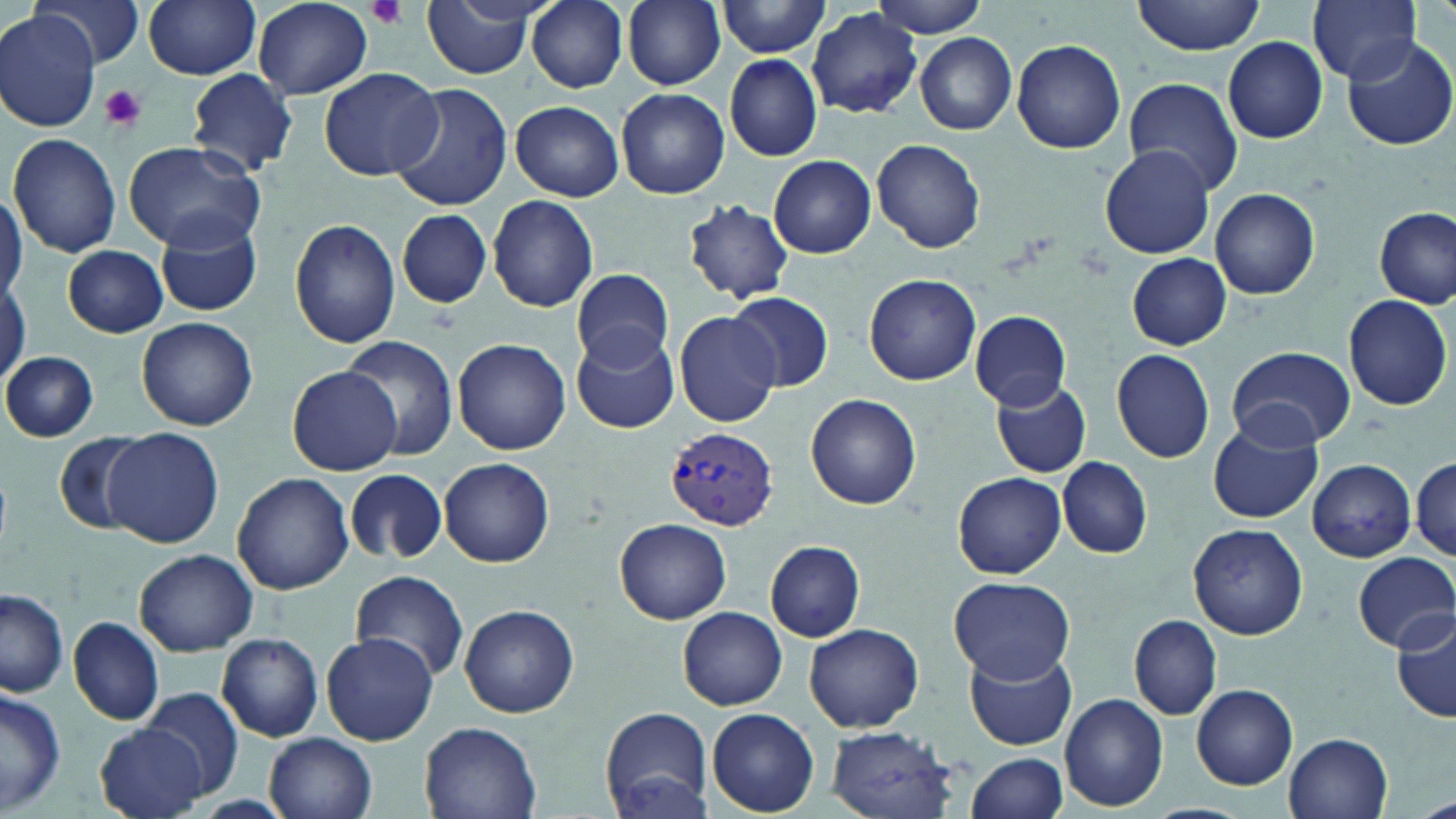
Approximate bounding boxes as named x1/y1/x2/y2 corners in pixels. Uninfected red blood cell locations: (x1=33, y1=0, x2=143, y2=70), (x1=143, y1=0, x2=262, y2=79), (x1=421, y1=0, x2=538, y2=79), (x1=527, y1=0, x2=628, y2=92), (x1=623, y1=0, x2=725, y2=89), (x1=863, y1=0, x2=996, y2=37), (x1=1131, y1=0, x2=1268, y2=56), (x1=1305, y1=0, x2=1425, y2=87), (x1=254, y1=1, x2=372, y2=100), (x1=716, y1=1, x2=834, y2=57), (x1=807, y1=8, x2=922, y2=118), (x1=0, y1=10, x2=103, y2=132), (x1=915, y1=33, x2=1016, y2=135), (x1=1338, y1=33, x2=1454, y2=149), (x1=1010, y1=38, x2=1126, y2=153), (x1=1223, y1=38, x2=1328, y2=143), (x1=723, y1=54, x2=823, y2=161), (x1=318, y1=67, x2=445, y2=181), (x1=187, y1=68, x2=298, y2=176), (x1=1124, y1=76, x2=1243, y2=195), (x1=387, y1=83, x2=514, y2=211), (x1=617, y1=88, x2=729, y2=200), (x1=510, y1=101, x2=624, y2=201), (x1=8, y1=134, x2=121, y2=259), (x1=873, y1=140, x2=985, y2=253), (x1=122, y1=141, x2=264, y2=254), (x1=1099, y1=145, x2=1216, y2=259), (x1=769, y1=155, x2=876, y2=258), (x1=1209, y1=187, x2=1320, y2=301), (x1=0, y1=189, x2=24, y2=306), (x1=488, y1=195, x2=598, y2=312), (x1=682, y1=199, x2=796, y2=305), (x1=1375, y1=207, x2=1454, y2=308), (x1=396, y1=208, x2=494, y2=308), (x1=155, y1=215, x2=263, y2=318), (x1=290, y1=218, x2=401, y2=349), (x1=62, y1=244, x2=169, y2=338), (x1=1126, y1=254, x2=1231, y2=349), (x1=571, y1=268, x2=675, y2=369), (x1=863, y1=273, x2=982, y2=386), (x1=0, y1=275, x2=28, y2=382), (x1=727, y1=292, x2=833, y2=392), (x1=1343, y1=293, x2=1452, y2=411), (x1=971, y1=309, x2=1070, y2=410), (x1=672, y1=310, x2=780, y2=427), (x1=138, y1=317, x2=258, y2=430), (x1=571, y1=325, x2=682, y2=435), (x1=337, y1=335, x2=462, y2=461), (x1=453, y1=339, x2=571, y2=455), (x1=1228, y1=346, x2=1354, y2=450), (x1=1110, y1=348, x2=1216, y2=463), (x1=1, y1=351, x2=98, y2=441), (x1=286, y1=366, x2=403, y2=476), (x1=991, y1=379, x2=1091, y2=479), (x1=806, y1=393, x2=922, y2=509), (x1=1207, y1=419, x2=1322, y2=524), (x1=103, y1=427, x2=224, y2=548), (x1=53, y1=433, x2=149, y2=537), (x1=1412, y1=456, x2=1455, y2=559), (x1=1058, y1=457, x2=1152, y2=558), (x1=439, y1=458, x2=554, y2=568), (x1=1306, y1=458, x2=1416, y2=563), (x1=345, y1=469, x2=447, y2=564), (x1=232, y1=471, x2=355, y2=595), (x1=953, y1=472, x2=1066, y2=579), (x1=616, y1=517, x2=731, y2=624), (x1=1188, y1=522, x2=1309, y2=640), (x1=765, y1=541, x2=866, y2=642), (x1=133, y1=548, x2=258, y2=655), (x1=1353, y1=552, x2=1455, y2=651), (x1=350, y1=571, x2=470, y2=683), (x1=948, y1=578, x2=1077, y2=682), (x1=1, y1=587, x2=68, y2=697), (x1=460, y1=603, x2=579, y2=717), (x1=678, y1=607, x2=787, y2=710), (x1=1392, y1=611, x2=1456, y2=726), (x1=1129, y1=615, x2=1222, y2=720), (x1=69, y1=617, x2=165, y2=726), (x1=804, y1=623, x2=924, y2=732), (x1=320, y1=632, x2=438, y2=746), (x1=217, y1=633, x2=324, y2=742), (x1=964, y1=648, x2=1079, y2=750), (x1=1192, y1=685, x2=1298, y2=789), (x1=0, y1=686, x2=65, y2=816), (x1=141, y1=690, x2=244, y2=799), (x1=1060, y1=693, x2=1169, y2=810), (x1=600, y1=705, x2=715, y2=816), (x1=708, y1=709, x2=819, y2=816), (x1=419, y1=720, x2=541, y2=819), (x1=98, y1=723, x2=209, y2=819), (x1=825, y1=727, x2=961, y2=817), (x1=266, y1=733, x2=378, y2=819), (x1=1285, y1=733, x2=1394, y2=819), (x1=966, y1=753, x2=1068, y2=819), (x1=1138, y1=803, x2=1254, y2=819). Plasmodium vivax-infected red blood cell locations: (x1=666, y1=427, x2=778, y2=529). Platelet locations: (x1=366, y1=0, x2=407, y2=30), (x1=100, y1=84, x2=147, y2=132). Slide-level diagnosis: Plasmodium vivax. Image is 1456×819 pixels. May-Grünwald-Giemsa stain. Optical microscopy. One field of a larger specimen. 1000x magnification. Thin blood smear.